Classify this cell by malaria status.
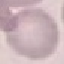
Uninfected.

Photographed with a smartphone camera at the microscope eyepiece. Thin smear of blood. Cell patch, automatically extracted from a larger field of view and resized to 64 × 64 pixels. Giemsa stain.